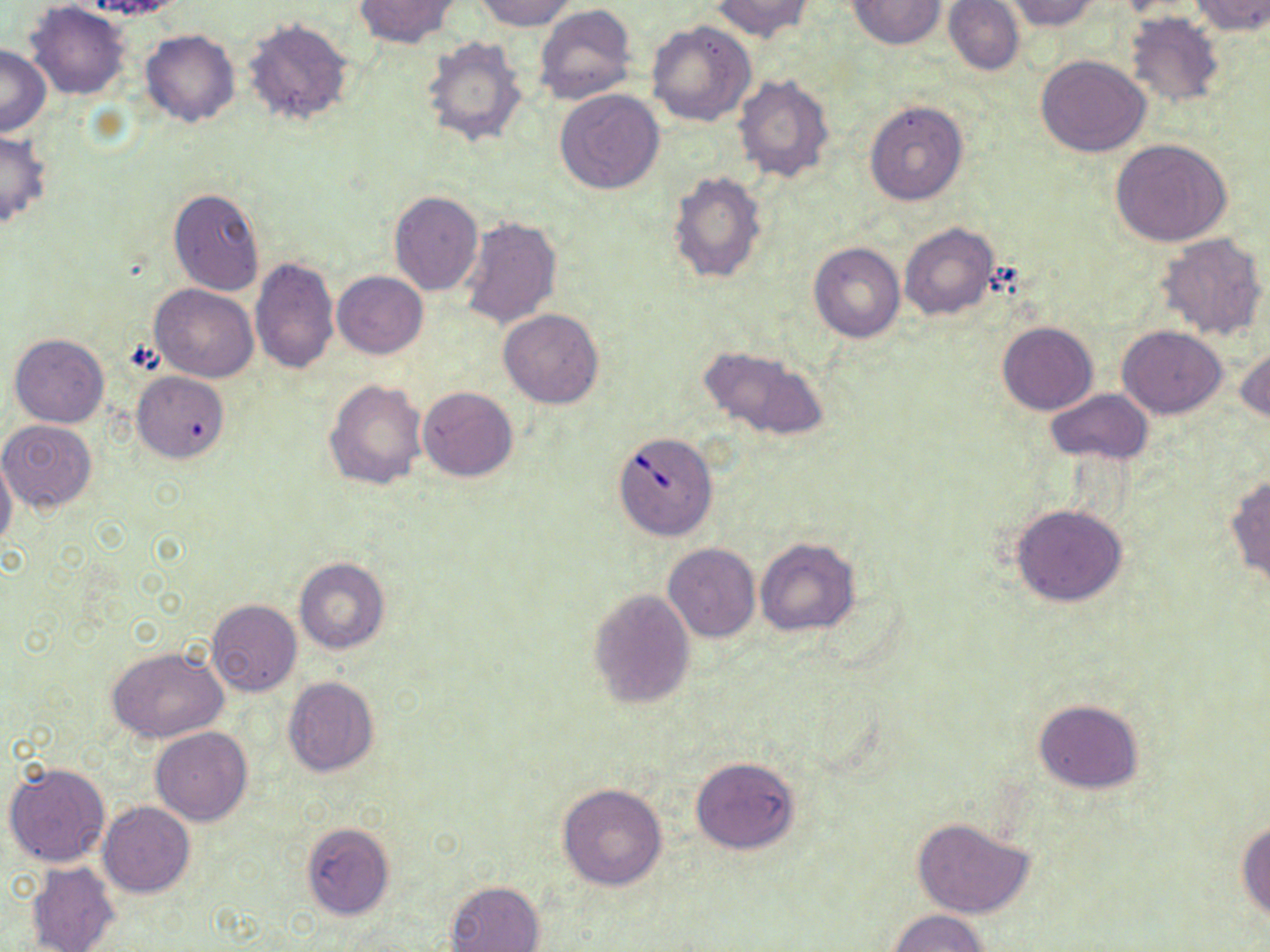

slide-level diagnosis = Babesia divergens
uninfected red blood cell locations = approximate bounding boxes as (x1, y1, x2, y2) in pixels: (69, 0, 188, 22), (353, 0, 458, 48), (473, 0, 576, 31), (711, 0, 814, 42), (945, 0, 1025, 76), (1004, 0, 1101, 32), (1190, 0, 1270, 35), (847, 1, 947, 49), (24, 2, 132, 100), (534, 5, 637, 106), (1125, 11, 1225, 109), (242, 17, 356, 128), (646, 20, 756, 127), (139, 29, 239, 127), (419, 34, 528, 147), (0, 44, 50, 136), (1036, 55, 1150, 157), (734, 74, 835, 183), (555, 89, 665, 193), (863, 99, 969, 206), (0, 130, 52, 230), (1111, 138, 1234, 248), (667, 170, 768, 284), (168, 188, 265, 296), (388, 190, 483, 296), (459, 215, 561, 330), (899, 223, 1000, 322), (1156, 232, 1269, 342), (809, 241, 905, 343), (250, 257, 338, 373), (332, 271, 428, 358), (150, 284, 258, 382), (499, 308, 603, 409), (997, 321, 1098, 415), (1117, 326, 1225, 418), (10, 333, 109, 427), (697, 343, 830, 442), (1235, 347, 1270, 424), (132, 373, 228, 463), (325, 378, 428, 492), (417, 386, 518, 481), (1045, 387, 1154, 466), (0, 419, 99, 512), (0, 456, 18, 554), (1225, 474, 1270, 587), (1010, 504, 1128, 606), (755, 538, 860, 637), (662, 543, 760, 642), (295, 558, 390, 655), (587, 589, 695, 709), (207, 599, 301, 695), (107, 647, 230, 741), (282, 677, 379, 776), (1032, 699, 1145, 793), (149, 727, 253, 825), (691, 756, 800, 854), (4, 761, 111, 867), (557, 784, 667, 889), (98, 802, 195, 897), (911, 817, 1034, 919), (1236, 818, 1270, 925), (300, 822, 394, 920), (26, 861, 121, 952), (445, 879, 546, 952), (886, 909, 991, 952)
image size = 1270×952 pixels
preparation = thin blood film
Babesia divergens-infected red blood cell locations = approximate bounding boxes as (x1, y1, x2, y2) in pixels: (613, 431, 717, 540)
modality = light microscopy
magnification = 1000x
field of view = one of a larger specimen
stain = May-Grünwald-Giemsa